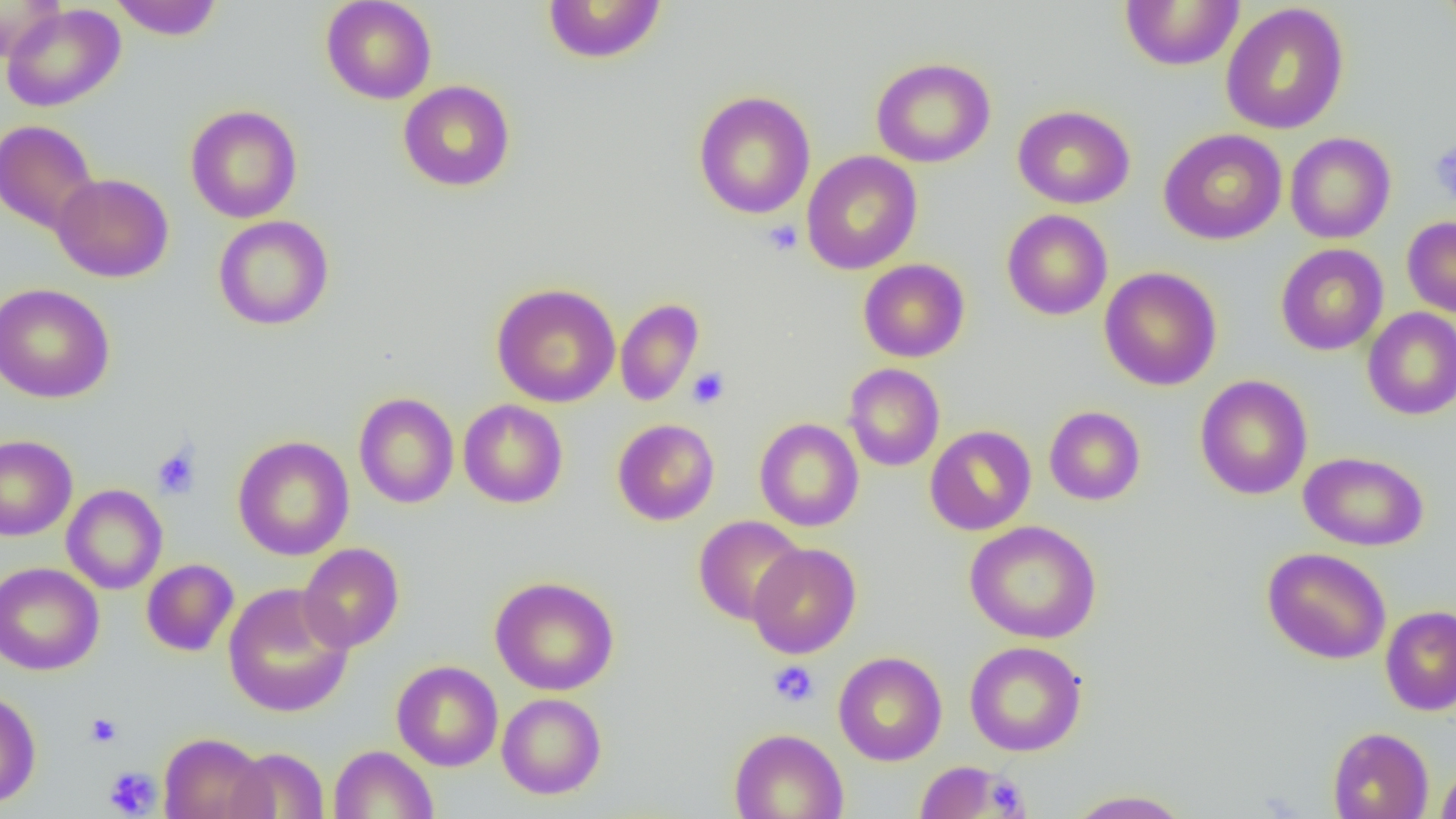

Approximate bounding boxes as [x1, y1, x2, y2] in pixels. Uninfected red blood cell locations: [109, 0, 224, 40], [321, 0, 437, 104], [542, 0, 667, 64], [1440, 0, 1456, 42], [0, 1, 65, 63], [1120, 1, 1244, 71], [1, 3, 126, 112], [1220, 3, 1350, 135], [870, 57, 996, 168], [398, 80, 516, 192], [693, 90, 815, 219], [186, 104, 302, 223], [1012, 105, 1135, 209], [0, 120, 100, 236], [1159, 128, 1287, 245], [1285, 132, 1396, 244], [802, 150, 922, 275], [51, 173, 174, 282], [1001, 209, 1113, 320], [213, 214, 334, 331], [1402, 216, 1456, 317], [1275, 244, 1389, 355], [858, 259, 970, 362], [1099, 266, 1222, 391], [0, 283, 114, 403], [491, 283, 621, 407], [615, 298, 704, 406], [1362, 307, 1456, 420], [843, 363, 945, 471], [1195, 374, 1313, 500], [353, 392, 459, 508], [458, 399, 568, 508], [1044, 406, 1145, 505], [754, 417, 864, 532], [612, 418, 720, 526], [924, 425, 1036, 535], [0, 434, 78, 541], [232, 435, 354, 561], [1299, 451, 1429, 552], [61, 484, 168, 595], [694, 515, 807, 625], [964, 521, 1102, 643], [298, 543, 404, 653], [747, 543, 862, 658], [1262, 547, 1391, 664], [141, 559, 239, 656], [0, 561, 104, 675], [489, 576, 619, 696], [223, 583, 354, 718], [1380, 605, 1456, 716], [965, 641, 1087, 756], [833, 651, 947, 766], [392, 660, 503, 771], [0, 690, 41, 810], [497, 693, 607, 799], [1328, 726, 1434, 819], [729, 728, 849, 819], [158, 732, 271, 819], [329, 744, 438, 819], [226, 747, 329, 818], [915, 761, 1010, 817], [1435, 762, 1456, 819], [1065, 789, 1193, 818]. Platelet locations: [1429, 139, 1456, 206], [763, 219, 803, 255], [687, 367, 730, 409], [152, 446, 201, 499], [768, 660, 819, 706], [86, 712, 122, 748], [103, 766, 161, 817], [985, 776, 1027, 816]. Slide-level diagnosis: no evidence of blood parasites. Image is 1456×819 pixels. Optical microscopy. Thin blood smear. Captured at 1000x magnification. One field of a larger specimen.